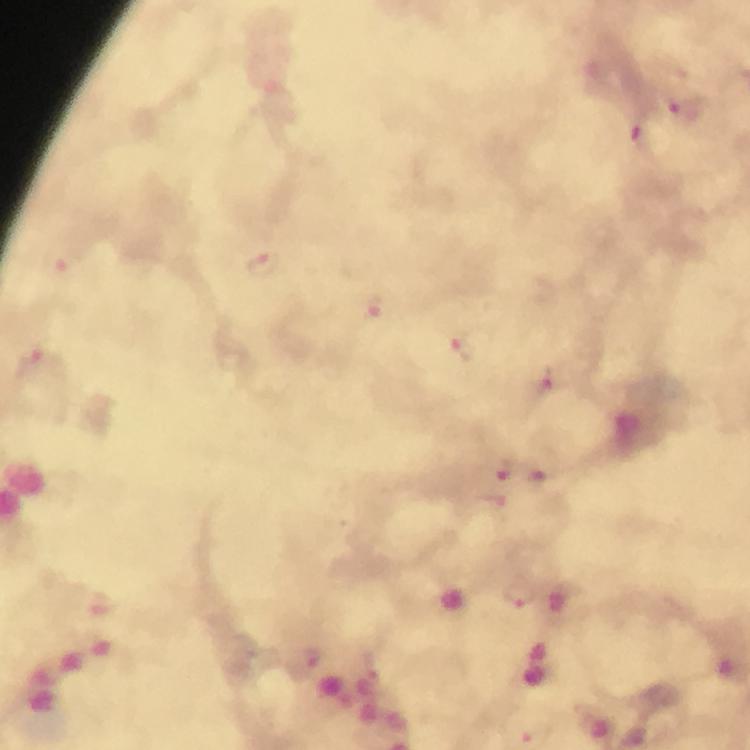 Approximate centers as [x, y] in pixels. Plasmodium parasite locations: [683, 112], [638, 137], [264, 263], [373, 306], [472, 345], [554, 378], [504, 471], [538, 478]. Giemsa-stained preparation. Image is 750×750 pixels. Photographed through the microscope with a smartphone camera. Cropped region of a single field of view. At 100x magnification. Immersion oil applied. From a malaria diagnostic workup. Thick smear.